Name the parasite shown.
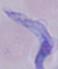
This is a trypanosome.

modality = micrograph
magnification = 1000x